Outline each Plasmodium ovale-infected red blood cell.
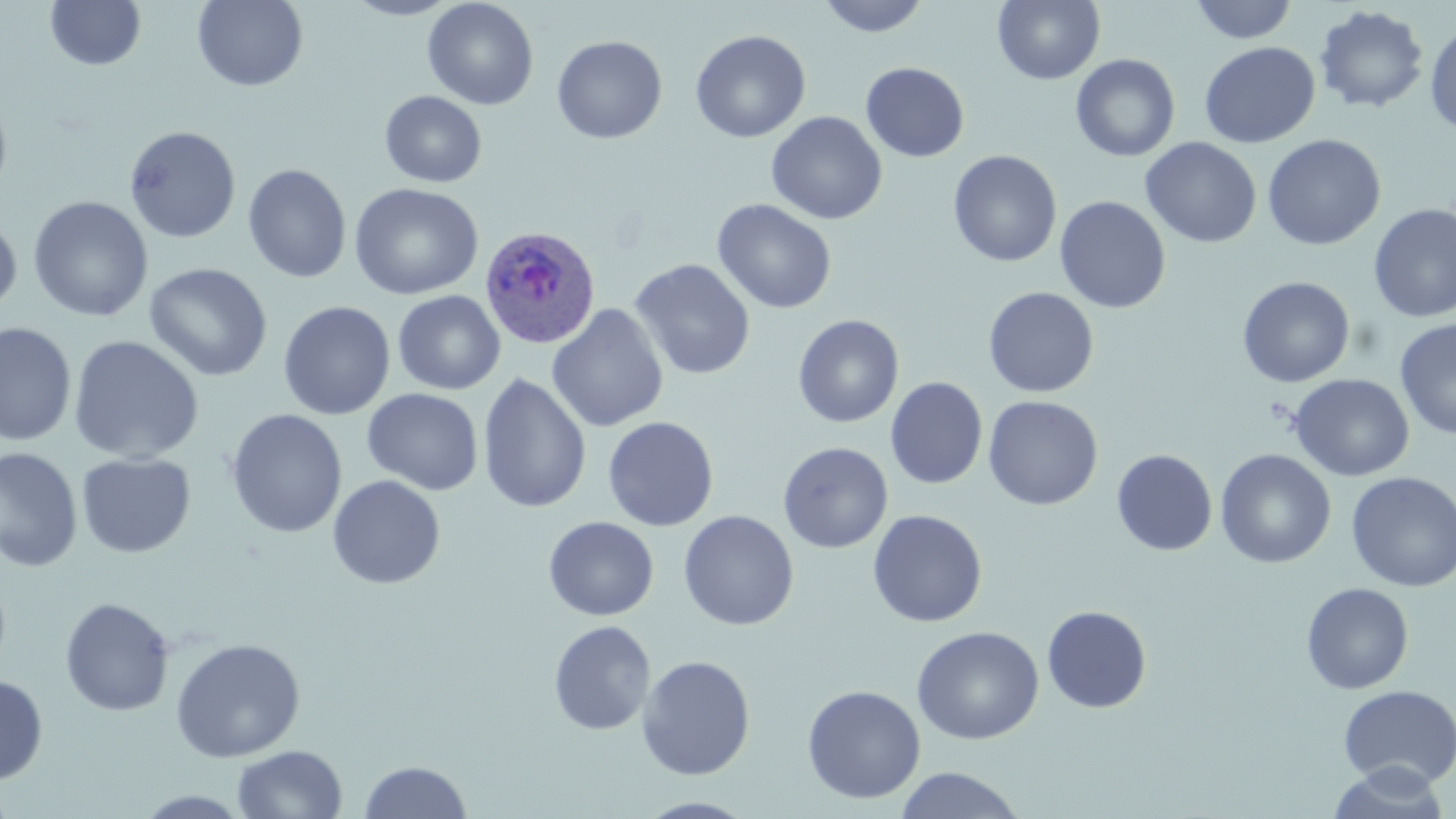
Approximate bounding boxes as named x1/y1/x2/y2 corners in pixels.
Plasmodium ovale-infected red blood cells: (x1=479, y1=225, x2=601, y2=349).

slide_level_diagnosis: Plasmodium ovale
stain: May-Grünwald-Giemsa
magnification: 1000x
uninfected_red_blood_cell_locations: 'approximate bounding boxes as named x1/y1/x2/y2 corners in pixels: (x1=192, y1=0, x2=308, y2=91), (x1=341, y1=0, x2=463, y2=20), (x1=422, y1=0, x2=539, y2=110), (x1=816, y1=0, x2=931, y2=37), (x1=993, y1=0, x2=1105, y2=85), (x1=1190, y1=0, x2=1298, y2=44), (x1=44, y1=1, x2=146, y2=71), (x1=1314, y1=5, x2=1429, y2=113), (x1=1425, y1=21, x2=1456, y2=137), (x1=690, y1=29, x2=810, y2=143), (x1=552, y1=35, x2=668, y2=144), (x1=1199, y1=42, x2=1320, y2=148), (x1=1071, y1=53, x2=1180, y2=161), (x1=860, y1=62, x2=969, y2=162), (x1=0, y1=90, x2=13, y2=205), (x1=379, y1=91, x2=487, y2=188), (x1=766, y1=111, x2=887, y2=225), (x1=124, y1=125, x2=241, y2=244), (x1=1262, y1=134, x2=1386, y2=250), (x1=1140, y1=137, x2=1261, y2=248), (x1=949, y1=150, x2=1062, y2=267), (x1=243, y1=164, x2=352, y2=283), (x1=349, y1=182, x2=484, y2=300), (x1=28, y1=196, x2=153, y2=323), (x1=1055, y1=196, x2=1171, y2=313), (x1=712, y1=198, x2=837, y2=315), (x1=1368, y1=203, x2=1456, y2=323), (x1=0, y1=212, x2=22, y2=315), (x1=629, y1=258, x2=756, y2=380), (x1=144, y1=262, x2=273, y2=382), (x1=1237, y1=276, x2=1355, y2=388), (x1=983, y1=287, x2=1099, y2=398), (x1=392, y1=290, x2=505, y2=395), (x1=278, y1=301, x2=395, y2=420), (x1=547, y1=303, x2=669, y2=433), (x1=793, y1=314, x2=904, y2=428), (x1=1395, y1=317, x2=1456, y2=440), (x1=0, y1=322, x2=76, y2=446), (x1=67, y1=335, x2=204, y2=464), (x1=477, y1=373, x2=592, y2=513), (x1=1289, y1=374, x2=1414, y2=481), (x1=885, y1=377, x2=987, y2=489), (x1=886, y1=381, x2=1096, y2=497), (x1=362, y1=388, x2=484, y2=495), (x1=983, y1=395, x2=1103, y2=511), (x1=226, y1=409, x2=347, y2=539), (x1=603, y1=416, x2=718, y2=531), (x1=778, y1=441, x2=893, y2=554), (x1=0, y1=447, x2=82, y2=572), (x1=1215, y1=449, x2=1336, y2=569), (x1=1111, y1=450, x2=1217, y2=556), (x1=76, y1=453, x2=196, y2=558), (x1=1346, y1=472, x2=1456, y2=592), (x1=327, y1=475, x2=446, y2=590), (x1=867, y1=509, x2=987, y2=628), (x1=678, y1=510, x2=799, y2=631), (x1=543, y1=516, x2=659, y2=621), (x1=1301, y1=582, x2=1414, y2=694), (x1=59, y1=597, x2=175, y2=717), (x1=1042, y1=605, x2=1152, y2=713), (x1=548, y1=620, x2=656, y2=735), (x1=911, y1=625, x2=1045, y2=745), (x1=170, y1=638, x2=306, y2=762), (x1=636, y1=655, x2=756, y2=780), (x1=0, y1=674, x2=49, y2=785), (x1=801, y1=684, x2=926, y2=804), (x1=1338, y1=685, x2=1455, y2=789), (x1=232, y1=745, x2=348, y2=818), (x1=358, y1=760, x2=472, y2=819), (x1=1327, y1=762, x2=1451, y2=818), (x1=893, y1=766, x2=1029, y2=818), (x1=133, y1=790, x2=255, y2=817), (x1=634, y1=796, x2=759, y2=818)'
modality: optical microscopy
field_of_view: one of a larger specimen
preparation: thin blood smear
image_size: 1456×819 pixels